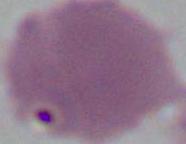

Captured at 1000x magnification. Photomicrograph. A red blood cell is seen.